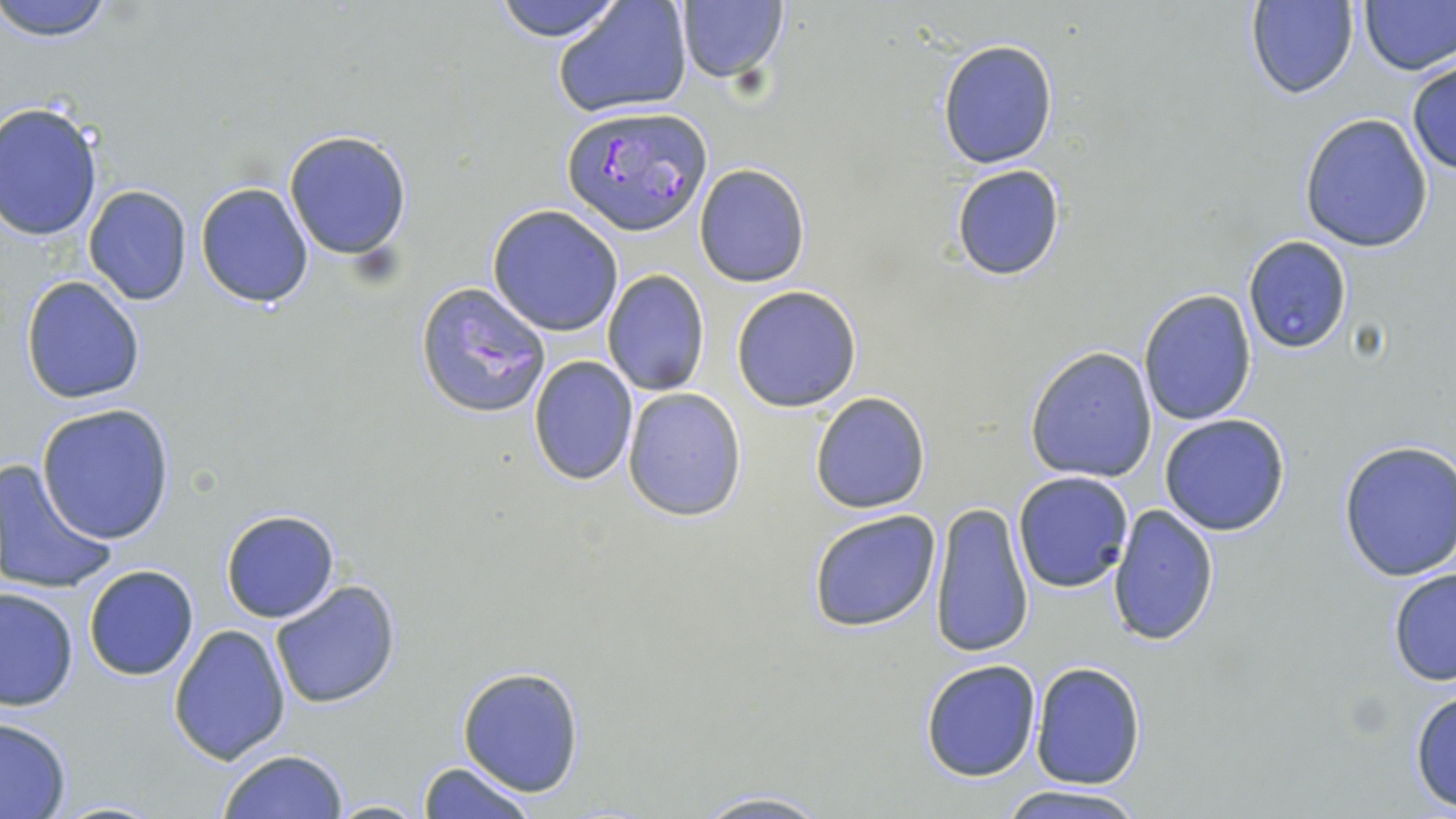
Summary:
  - Coordinate format: approximate bounding boxes as (x1, y1, x2, y2) in pixels
  - Uninfected red blood cell locations: (0, 0, 114, 43), (489, 0, 631, 43), (552, 0, 693, 119), (674, 0, 789, 90), (1356, 0, 1455, 75), (1245, 1, 1359, 100), (936, 39, 1059, 170), (1405, 58, 1456, 177), (0, 102, 103, 241), (1299, 112, 1435, 253), (284, 129, 413, 262), (693, 164, 811, 287), (950, 164, 1065, 281), (195, 182, 314, 310), (82, 184, 193, 304), (487, 203, 623, 337), (1244, 237, 1352, 354), (600, 269, 712, 396), (21, 276, 146, 406), (731, 285, 863, 412), (1137, 289, 1256, 427), (1025, 346, 1158, 482), (527, 355, 640, 486), (621, 387, 748, 522), (809, 390, 932, 514), (37, 404, 176, 545), (1159, 415, 1291, 536), (1337, 439, 1456, 583), (0, 457, 119, 596), (1011, 471, 1135, 593), (929, 501, 1036, 659), (1106, 503, 1220, 648), (806, 507, 942, 634), (219, 508, 340, 623), (82, 564, 199, 681), (1387, 564, 1455, 686), (268, 579, 403, 707), (1, 586, 78, 712), (166, 624, 291, 764), (919, 659, 1042, 782), (1028, 661, 1146, 789), (457, 666, 585, 797), (1408, 686, 1456, 812), (0, 716, 73, 818), (217, 747, 350, 818), (417, 759, 538, 819), (998, 784, 1151, 818), (689, 791, 835, 819), (324, 798, 430, 817)
  - Plasmodium falciparum-infected red blood cell locations: (562, 106, 711, 237), (414, 281, 551, 418)
  - Slide-level diagnosis: Plasmodium falciparum
  - Stain: May-Grünwald-Giemsa
  - Modality: light microscopy
  - Preparation: thin blood film
  - Image size: 1456×819 pixels
  - Magnification: 1000x
  - Field of view: single